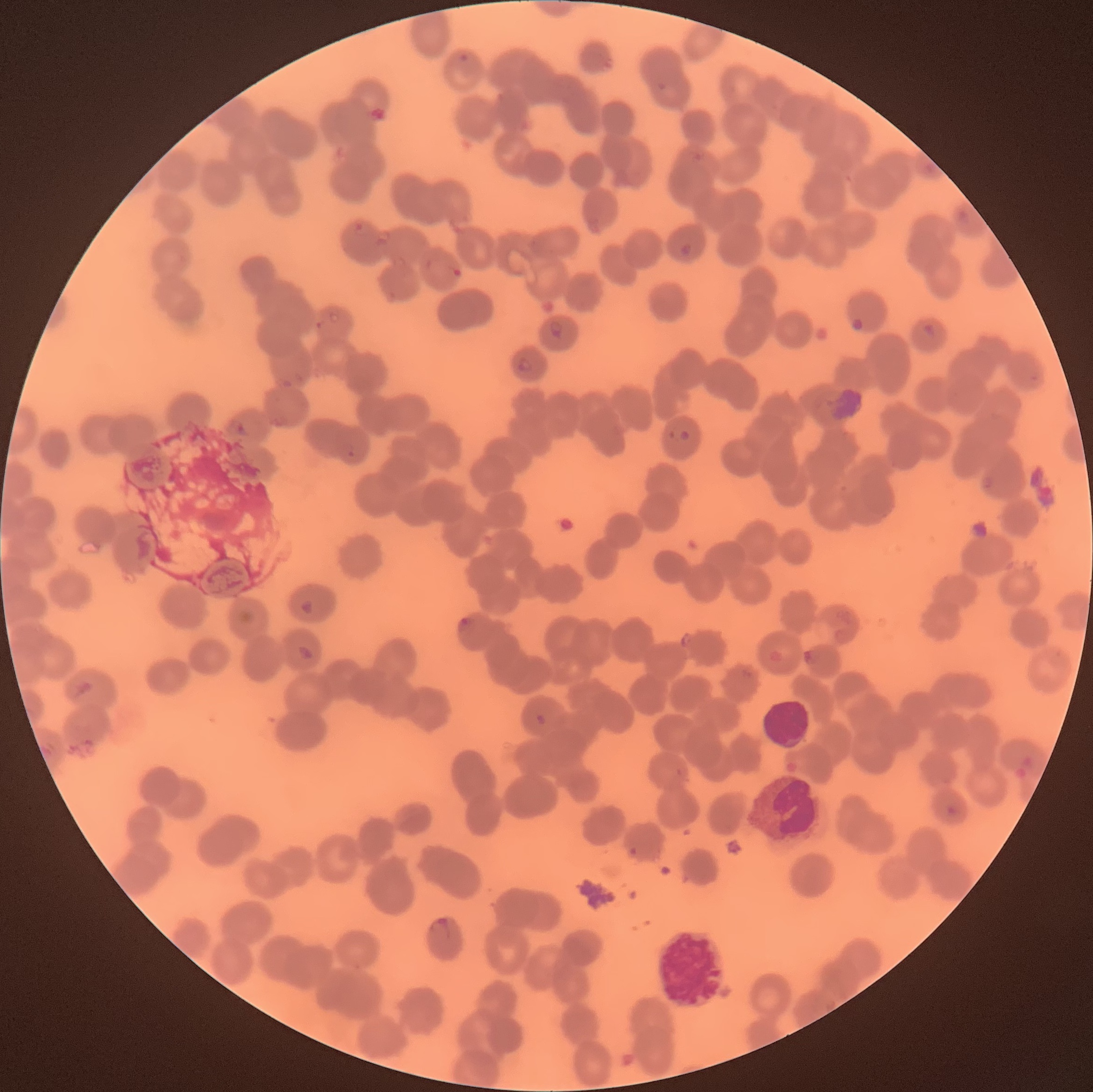

Summary:
  - Coordinate format: approximate bounding boxes as (x1, y1, x2, y2) in pixels
  - Plasmodium parasite locations: (677, 241, 696, 259), (548, 320, 565, 339), (922, 321, 936, 339), (515, 356, 533, 375), (679, 428, 690, 442), (300, 599, 315, 617), (297, 643, 315, 663), (63, 677, 95, 701), (534, 713, 548, 727), (945, 804, 961, 820), (429, 916, 452, 941)
  - White blood cell locations: (763, 699, 810, 750), (750, 771, 826, 844), (657, 921, 726, 1013)
  - Red blood cell morphology: rouleaux formation
  - Preparation: thin blood film
  - Modality: light microscopy
  - Image size: 1093×1092 pixels